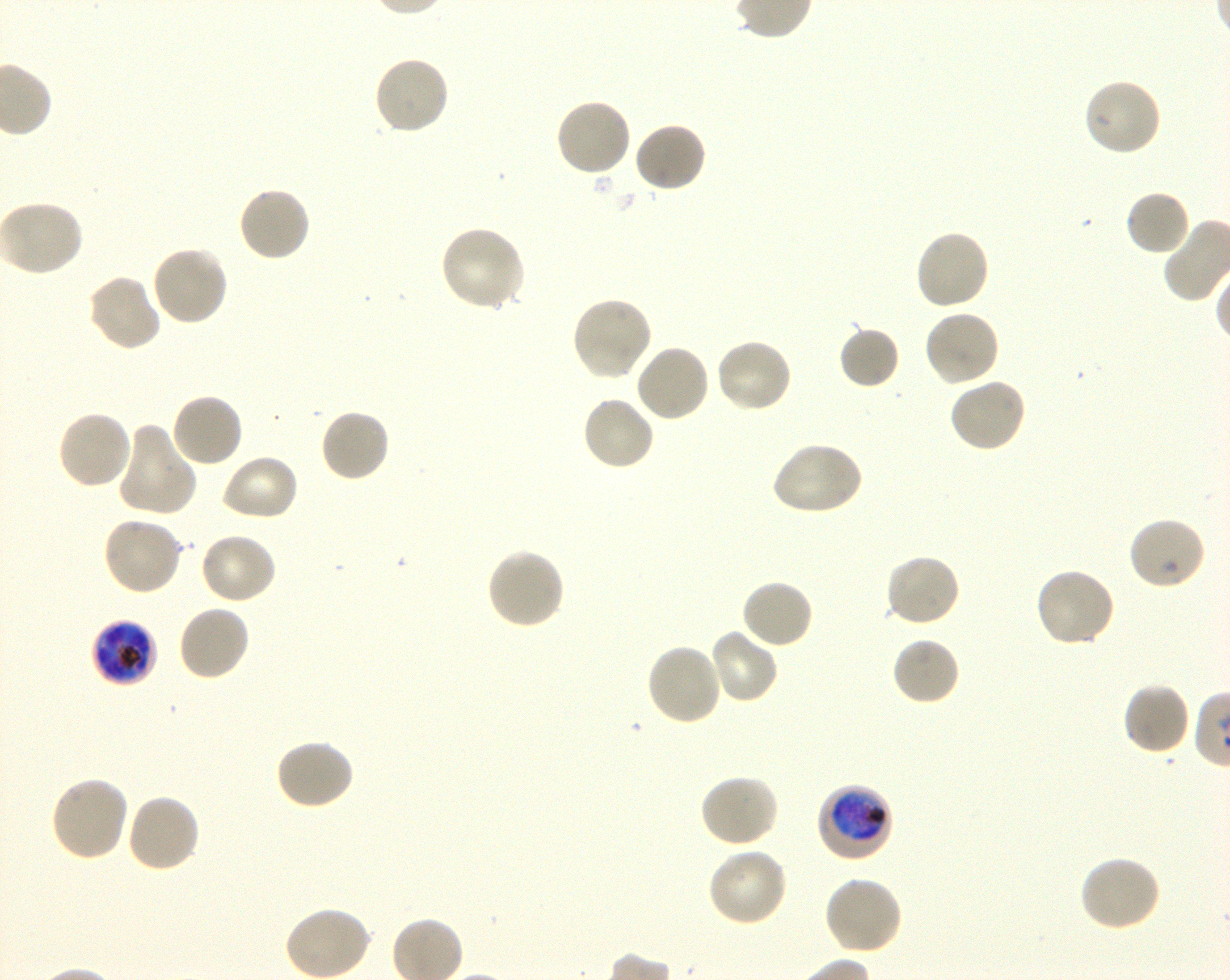

Approximate bounding boxes as {x1, y1, x2, y2} in pixels. Not every red blood cell is marked. A life-cycle stage — or a range of stages, where the recorded stages span more than one — follows each staged infected red blood cell.
Summary:
  - Locations of uninfected red blood cells: {371, 55, 451, 136}, {1082, 77, 1162, 158}, {553, 97, 632, 178}, {634, 122, 708, 194}, {236, 185, 312, 263}, {1124, 189, 1192, 257}, {1, 199, 86, 276}, {439, 225, 527, 313}, {914, 228, 991, 311}, {151, 244, 229, 327}, {86, 273, 162, 353}, {569, 296, 653, 381}, {922, 308, 1001, 388}, {838, 325, 901, 390}, {714, 338, 793, 415}, {634, 343, 710, 424}, {948, 377, 1027, 454}, {170, 392, 245, 469}, {581, 395, 656, 473}, {319, 408, 392, 483}, {55, 409, 134, 491}, {116, 422, 198, 519}, {771, 441, 864, 517}, {219, 453, 299, 522}, {101, 515, 183, 596}, {1128, 516, 1207, 591}, {198, 532, 278, 605}, {484, 547, 565, 631}, {883, 553, 962, 629}, {1032, 566, 1116, 648}, {741, 578, 815, 650}, {175, 603, 251, 683}, {708, 627, 779, 705}, {892, 636, 961, 706}, {644, 642, 723, 727}, {1121, 681, 1191, 756}, {274, 739, 356, 811}, {699, 773, 779, 848}, {49, 774, 130, 862}, {124, 792, 201, 873}, {706, 846, 789, 927}, {1078, 855, 1162, 933}, {823, 875, 904, 956}, {285, 905, 372, 980}
  - Locations of infected red blood cells: {89, 621, 159, 686} late trophozoite to late schizont; {817, 783, 893, 864} early trophozoite to early schizont
  - Field of view: one from this slide
  - Preparation: thin blood smear
  - Donor blood group: O+
  - Stain: Giemsa
  - Image size: 1230×980 pixels
  - Objective: 100x, oil immersion, numerical aperture 1.30
  - Culture: in-vitro Plasmodium falciparum strain 3D7, shaking